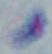
magnification = 1000x
modality = micrograph
identification = Toxoplasma gondii